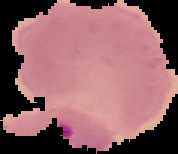
Summary:
  - Malaria status: parasitized
  - Image size: 178×154 pixels
  - Image type: segmented cell region with the area outside set to black
  - Preparation: thin blood smear